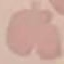

Malaria status: uninfected. Automatically extracted cell patch, resized to 64 × 64 pixels. Thin smear of blood. Giemsa stain. Photographed with a smartphone camera at the microscope eyepiece.